Assess for malaria.
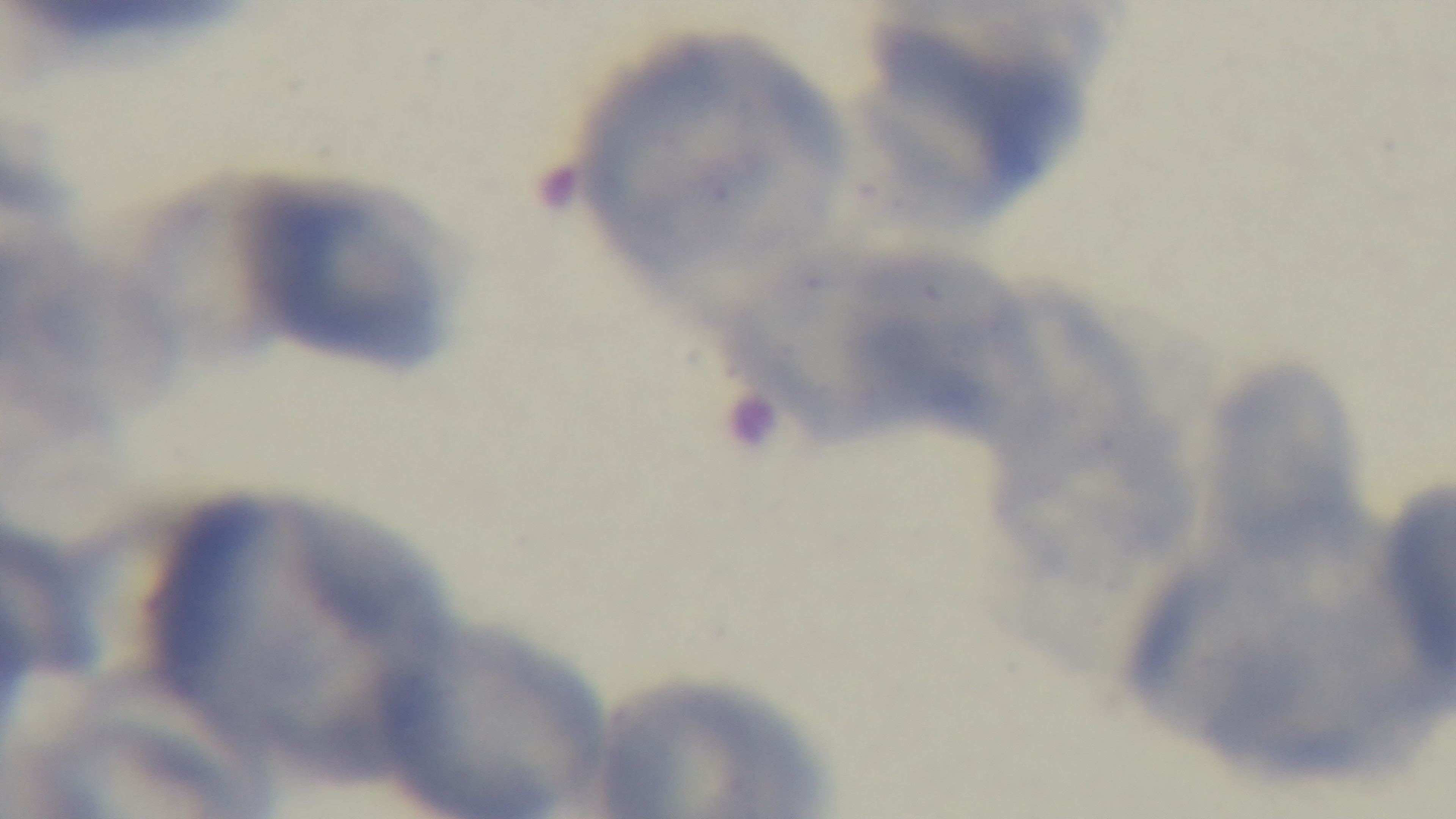

Uninfected.

Summary:
  - Preparation: thin
  - Field of view: one from the slide
  - Objective: 100x oil immersion
  - Stain: Giemsa
  - Modality: light microscopy
  - Capture: mounted 4K digital camera